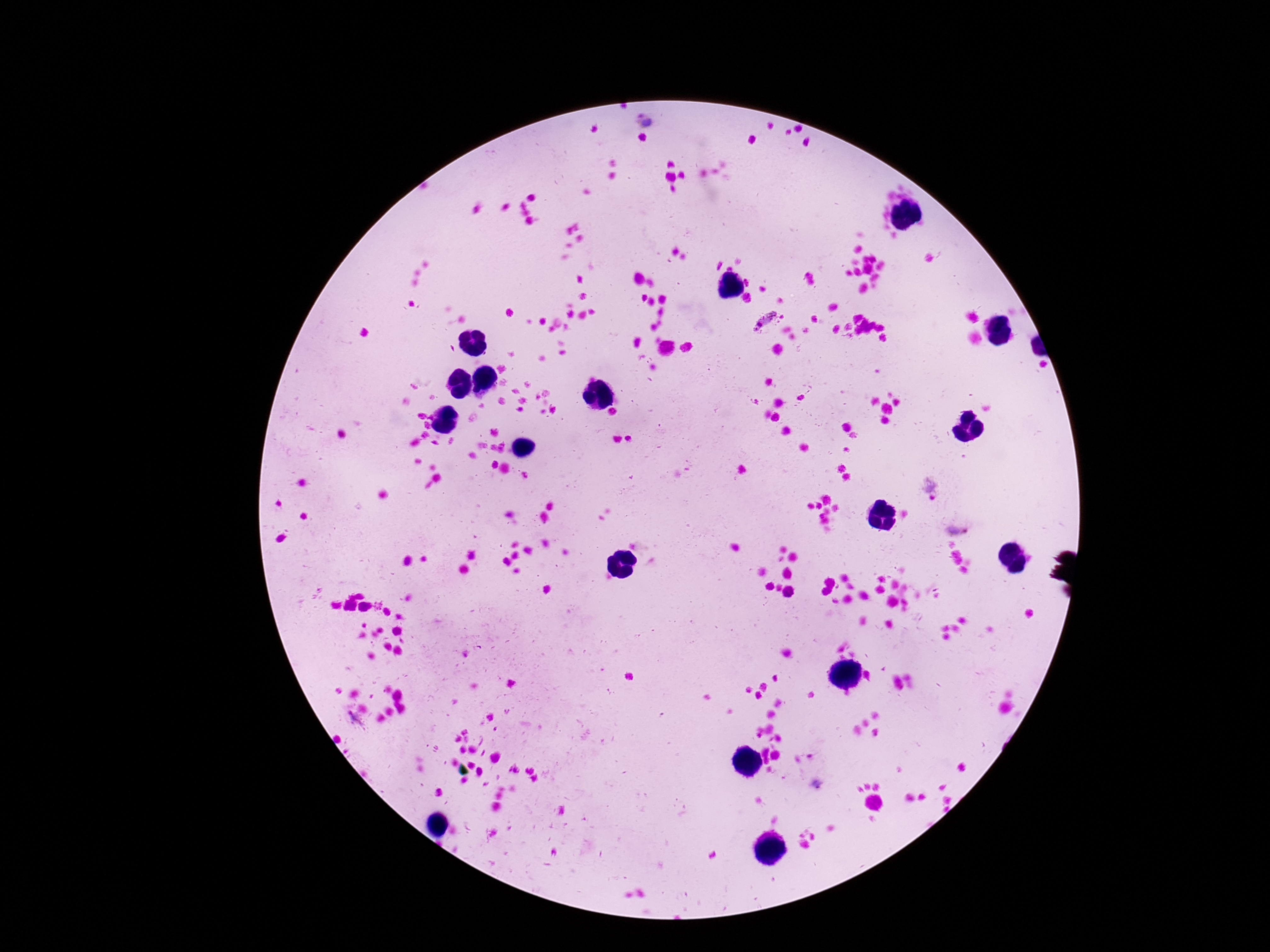
Approximate centers as (x, y) in pixels. Plasmodium parasite locations: (646, 121), (764, 321), (931, 489), (957, 527). 100x magnification. Smartphone photograph taken through the microscope eyepiece. Patient malaria status: infected. Thick blood film. Image is 1270×952 pixels. One field from this slide. Giemsa-stained preparation.